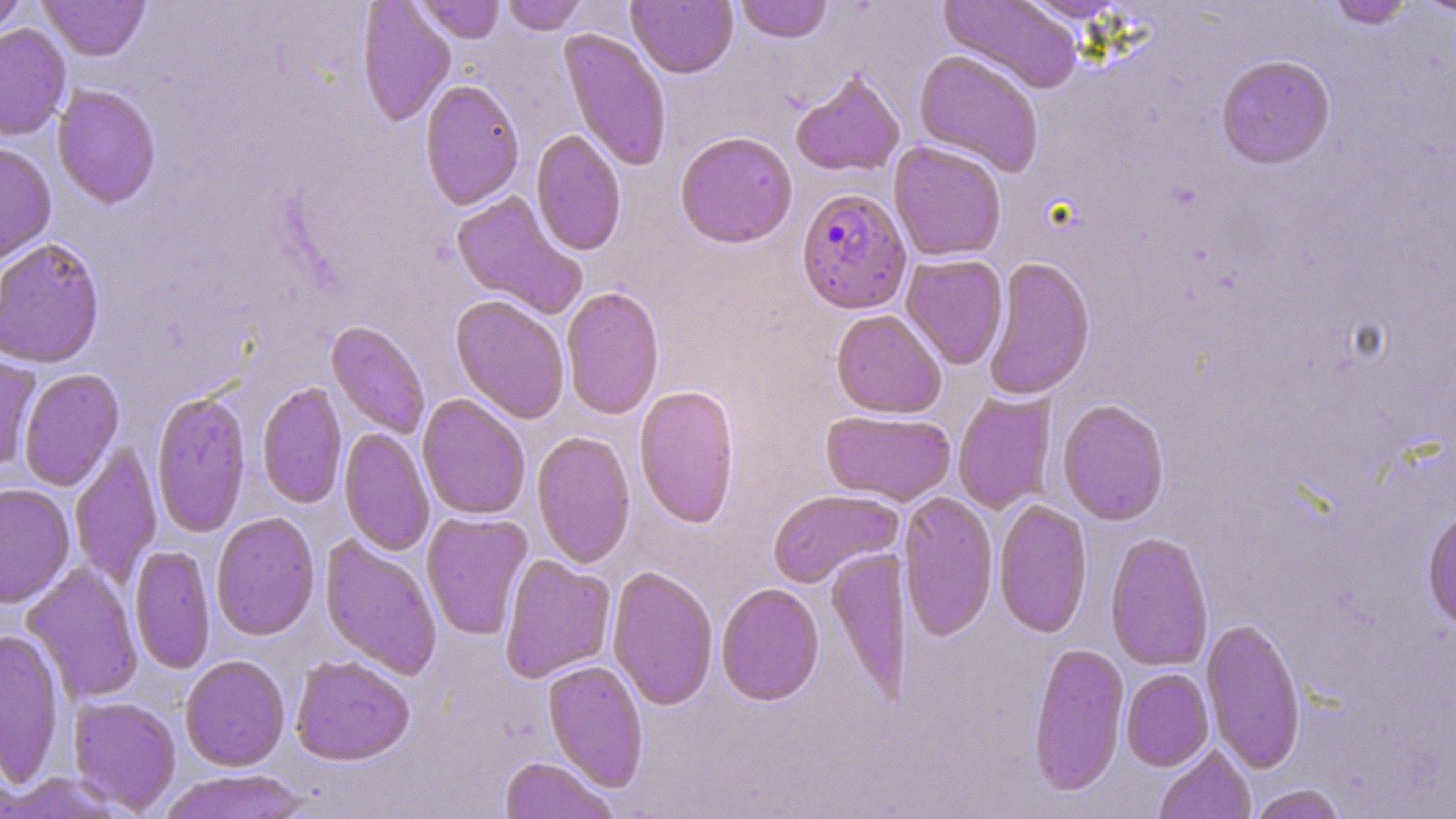

slide-level diagnosis = Plasmodium falciparum
stain = May-Grünwald-Giemsa
field of view = single
preparation = thin blood smear
uninfected red blood cell locations = approximate bounding boxes as named x1/y1/x2/y2 corners in pixels: (x1=0, y1=0, x2=29, y2=38), (x1=39, y1=0, x2=150, y2=61), (x1=501, y1=0, x2=587, y2=35), (x1=627, y1=0, x2=738, y2=80), (x1=735, y1=0, x2=833, y2=45), (x1=939, y1=0, x2=1084, y2=96), (x1=1016, y1=0, x2=1134, y2=23), (x1=1327, y1=0, x2=1416, y2=30), (x1=1412, y1=0, x2=1455, y2=18), (x1=356, y1=1, x2=456, y2=128), (x1=416, y1=1, x2=504, y2=44), (x1=0, y1=24, x2=71, y2=142), (x1=558, y1=29, x2=672, y2=173), (x1=914, y1=51, x2=1044, y2=179), (x1=1216, y1=56, x2=1336, y2=171), (x1=790, y1=69, x2=906, y2=180), (x1=419, y1=80, x2=524, y2=212), (x1=52, y1=85, x2=161, y2=210), (x1=530, y1=130, x2=626, y2=257), (x1=675, y1=133, x2=798, y2=250), (x1=889, y1=142, x2=1006, y2=262), (x1=0, y1=143, x2=56, y2=268), (x1=450, y1=191, x2=586, y2=317), (x1=0, y1=239, x2=105, y2=369), (x1=901, y1=255, x2=1009, y2=370), (x1=983, y1=257, x2=1096, y2=402), (x1=561, y1=287, x2=664, y2=421), (x1=449, y1=296, x2=569, y2=424), (x1=831, y1=310, x2=946, y2=419), (x1=325, y1=321, x2=430, y2=440), (x1=0, y1=351, x2=41, y2=471), (x1=17, y1=370, x2=123, y2=491), (x1=256, y1=382, x2=347, y2=509), (x1=634, y1=385, x2=740, y2=529), (x1=151, y1=392, x2=252, y2=537), (x1=952, y1=392, x2=1057, y2=514), (x1=417, y1=395, x2=530, y2=521), (x1=1057, y1=400, x2=1170, y2=526), (x1=820, y1=410, x2=957, y2=506), (x1=339, y1=428, x2=434, y2=556), (x1=532, y1=431, x2=636, y2=569), (x1=70, y1=444, x2=162, y2=588), (x1=0, y1=484, x2=75, y2=609), (x1=768, y1=489, x2=903, y2=589), (x1=898, y1=492, x2=998, y2=643), (x1=993, y1=499, x2=1092, y2=639), (x1=1422, y1=507, x2=1456, y2=635), (x1=422, y1=512, x2=533, y2=641), (x1=210, y1=513, x2=320, y2=642), (x1=1105, y1=533, x2=1214, y2=672), (x1=320, y1=536, x2=442, y2=680), (x1=129, y1=545, x2=215, y2=675), (x1=825, y1=548, x2=912, y2=704), (x1=499, y1=555, x2=616, y2=684), (x1=22, y1=563, x2=143, y2=703), (x1=607, y1=566, x2=718, y2=710), (x1=716, y1=583, x2=825, y2=707), (x1=1201, y1=618, x2=1306, y2=773), (x1=0, y1=629, x2=65, y2=788), (x1=1028, y1=643, x2=1129, y2=797), (x1=179, y1=655, x2=290, y2=771), (x1=291, y1=656, x2=415, y2=767), (x1=542, y1=660, x2=648, y2=792), (x1=1121, y1=669, x2=1214, y2=772), (x1=68, y1=696, x2=182, y2=815), (x1=1154, y1=744, x2=1255, y2=819), (x1=499, y1=757, x2=617, y2=818), (x1=159, y1=770, x2=311, y2=819), (x1=1, y1=771, x2=126, y2=818), (x1=1248, y1=785, x2=1349, y2=819)
magnification = 1000x
image size = 1456×819 pixels
Plasmodium falciparum-infected red blood cell locations = approximate bounding boxes as named x1/y1/x2/y2 corners in pixels: (x1=795, y1=188, x2=912, y2=316)
modality = optical microscopy